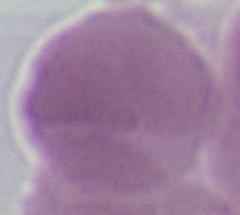

Captured at 1000x magnification. A red blood cell is shown. Photomicrograph.